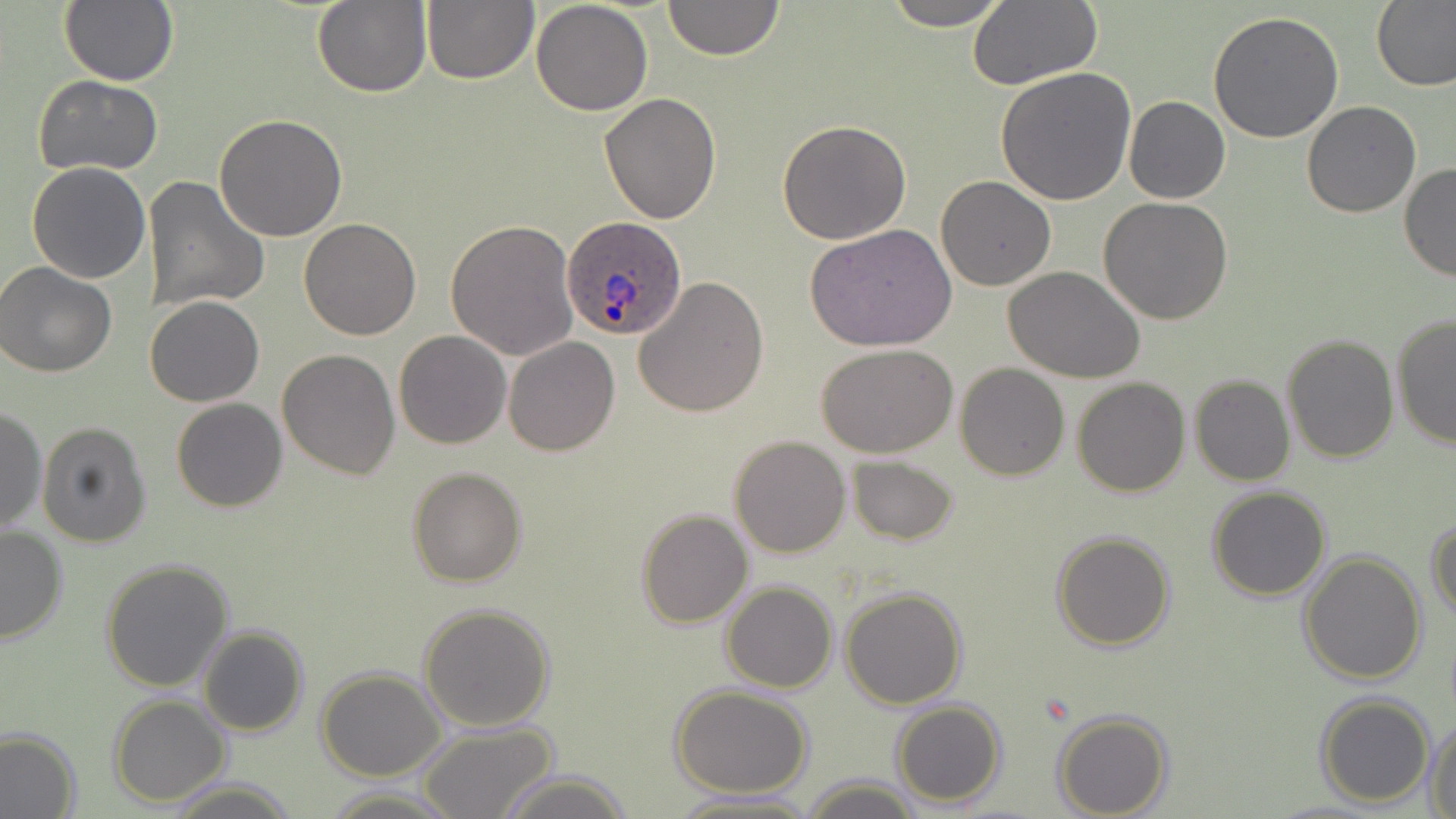
Approximate bounding boxes as named x1/y1/x2/y2 corners in pixels. Plasmodium ovale-infected red blood cell locations: (x1=563, y1=215, x2=688, y2=340). Uninfected red blood cell locations: (x1=60, y1=0, x2=179, y2=88), (x1=663, y1=0, x2=783, y2=61), (x1=883, y1=0, x2=1013, y2=29), (x1=312, y1=1, x2=432, y2=98), (x1=421, y1=1, x2=537, y2=84), (x1=529, y1=1, x2=653, y2=116), (x1=1372, y1=1, x2=1456, y2=93), (x1=967, y1=2, x2=1102, y2=89), (x1=1208, y1=10, x2=1345, y2=143), (x1=994, y1=66, x2=1137, y2=206), (x1=34, y1=75, x2=165, y2=176), (x1=598, y1=93, x2=721, y2=224), (x1=1124, y1=96, x2=1231, y2=204), (x1=1301, y1=101, x2=1421, y2=218), (x1=214, y1=115, x2=348, y2=241), (x1=777, y1=120, x2=913, y2=245), (x1=25, y1=162, x2=152, y2=284), (x1=1398, y1=163, x2=1456, y2=282), (x1=141, y1=176, x2=270, y2=316), (x1=936, y1=176, x2=1056, y2=290), (x1=1098, y1=197, x2=1234, y2=324), (x1=298, y1=217, x2=422, y2=339), (x1=446, y1=219, x2=580, y2=362), (x1=809, y1=224, x2=958, y2=353), (x1=0, y1=261, x2=118, y2=378), (x1=1005, y1=268, x2=1146, y2=385), (x1=634, y1=276, x2=769, y2=417), (x1=144, y1=296, x2=264, y2=406), (x1=1390, y1=312, x2=1455, y2=451), (x1=394, y1=330, x2=511, y2=450), (x1=1280, y1=334, x2=1398, y2=463), (x1=503, y1=337, x2=620, y2=456), (x1=818, y1=347, x2=956, y2=459), (x1=277, y1=349, x2=401, y2=479), (x1=955, y1=363, x2=1070, y2=481), (x1=1189, y1=375, x2=1294, y2=487), (x1=1072, y1=377, x2=1190, y2=498), (x1=171, y1=398, x2=288, y2=512), (x1=1, y1=406, x2=46, y2=534), (x1=37, y1=422, x2=153, y2=547), (x1=729, y1=435, x2=851, y2=557), (x1=847, y1=454, x2=958, y2=545), (x1=407, y1=466, x2=526, y2=587), (x1=1207, y1=487, x2=1331, y2=602), (x1=635, y1=508, x2=753, y2=628), (x1=1426, y1=514, x2=1456, y2=624), (x1=0, y1=524, x2=68, y2=644), (x1=1050, y1=530, x2=1176, y2=651), (x1=1298, y1=549, x2=1427, y2=685), (x1=99, y1=557, x2=234, y2=691), (x1=720, y1=580, x2=838, y2=694), (x1=840, y1=587, x2=967, y2=709), (x1=417, y1=602, x2=557, y2=732), (x1=197, y1=625, x2=309, y2=737), (x1=316, y1=669, x2=445, y2=780), (x1=671, y1=685, x2=814, y2=797), (x1=1314, y1=693, x2=1436, y2=807), (x1=108, y1=695, x2=230, y2=806), (x1=892, y1=699, x2=1007, y2=807), (x1=1051, y1=711, x2=1173, y2=819), (x1=1426, y1=716, x2=1456, y2=818), (x1=415, y1=721, x2=560, y2=819), (x1=0, y1=728, x2=81, y2=819), (x1=494, y1=769, x2=632, y2=819), (x1=799, y1=776, x2=923, y2=818), (x1=164, y1=779, x2=298, y2=816), (x1=322, y1=786, x2=455, y2=817), (x1=666, y1=792, x2=817, y2=819). Slide-level diagnosis: Plasmodium ovale. One field of a larger specimen. Image is 1456×819 pixels. May-Grünwald-Giemsa-stained preparation. Thin blood smear. Light microscopy. 1000x magnification.